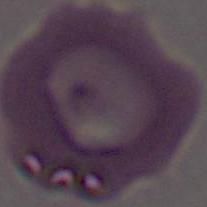 A red blood cell is shown. Captured at 1000x magnification. Micrograph.